Comment on the morphology of the erythrocytes.
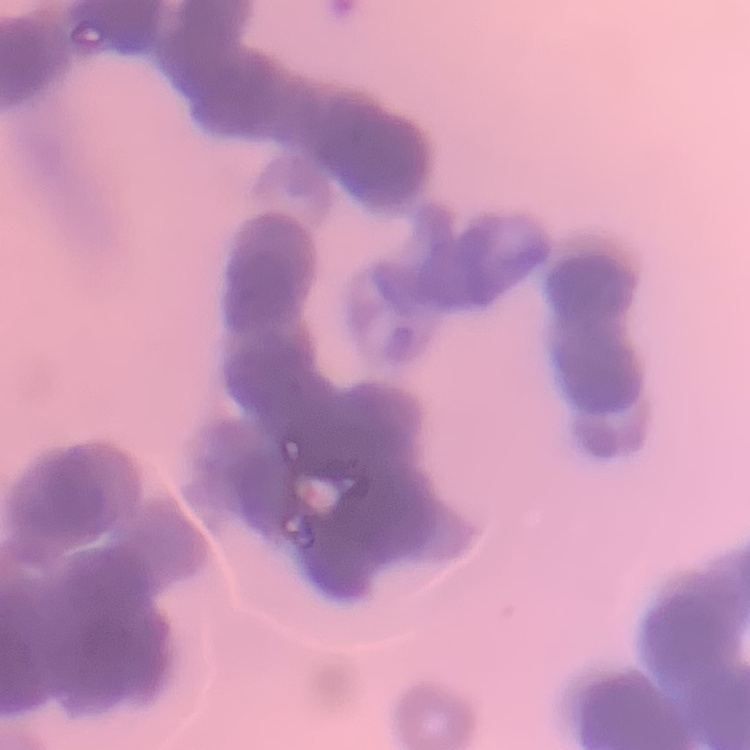
They show rouleaux formation.

Summary:
  - Image type: one tile cut from a larger photomicrograph
  - Stain: Field's or Giemsa
  - Preparation: thin peripheral smear